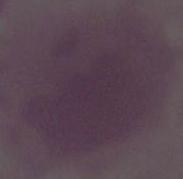
Captured at 1000x magnification. Micrograph. A red blood cell is seen.